Point out each Plasmodium parasite and each leukocyte.
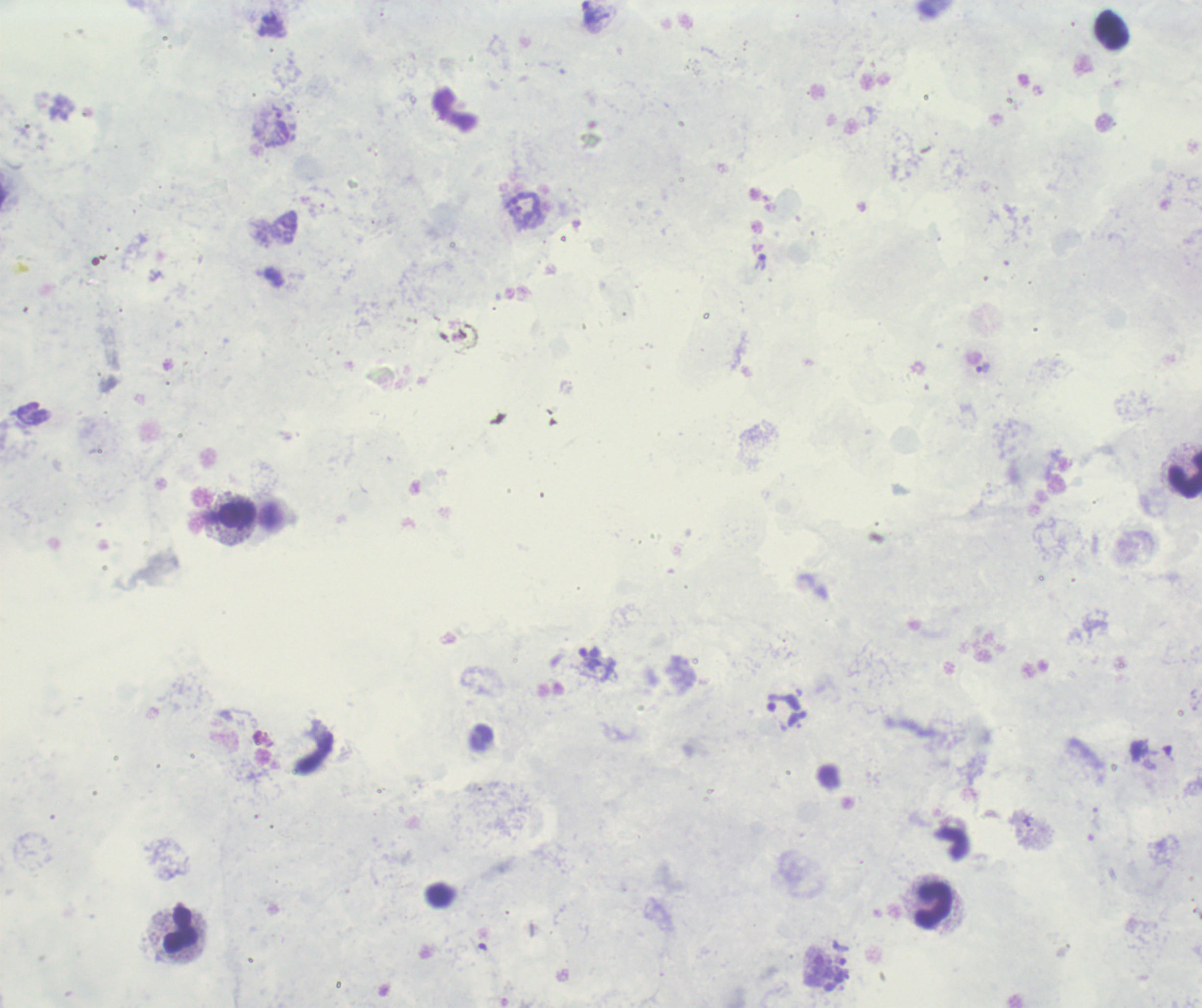

Approximate centers as {x, y} in pixels.
Trophozoites: {276, 111}, {983, 368}, {1027, 822}.
No schizont or gametocyte forms observed.
Leukocytes: {1184, 475}, {238, 516}, {934, 905}, {181, 931}.

Background quality: poor. Previously used in an actual diagnosis. Romanowsky stain. Single field of view. Image is 1202×1008 pixels. 100x magnification. Thick smear of blood.